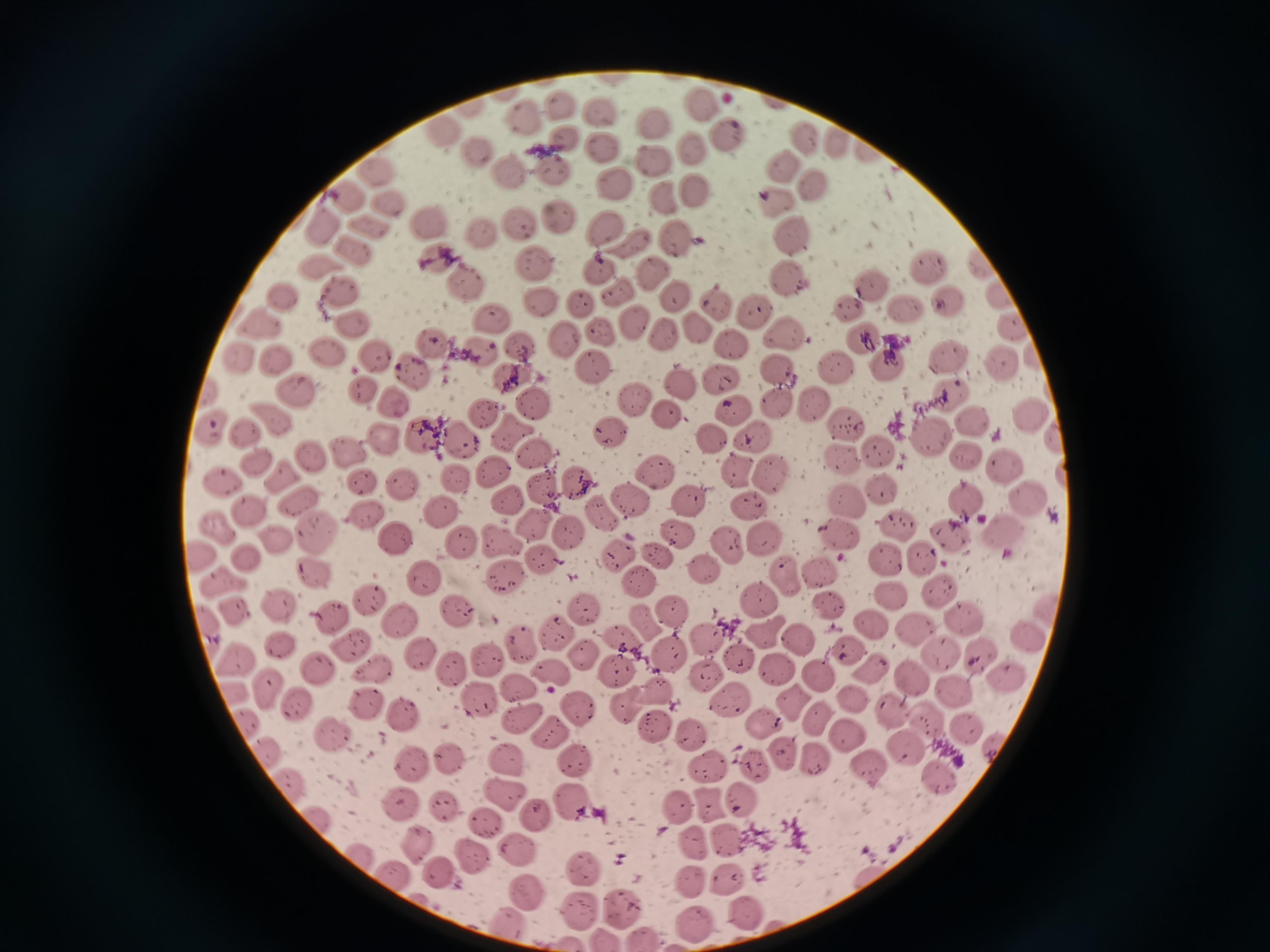 Approximate centers as (x, y) in pixels. Cell locations: (558, 106), (702, 106), (598, 114), (523, 121), (656, 121), (726, 132), (444, 133), (568, 137), (806, 138), (837, 141), (477, 149), (691, 149), (866, 151), (602, 153), (652, 163), (784, 166), (558, 170), (370, 171), (506, 172), (607, 182), (815, 184), (696, 191), (663, 196), (351, 197), (390, 199), (778, 199), (559, 217), (430, 221), (372, 223), (516, 226), (601, 227), (326, 228), (476, 231), (795, 236), (678, 237), (630, 246), (354, 248), (435, 258), (979, 263), (534, 264), (926, 268), (321, 269), (596, 269), (652, 270), (785, 278), (462, 282), (871, 284), (343, 289), (621, 290), (672, 293), (997, 293), (283, 296), (947, 298), (543, 305), (718, 306), (901, 306), (579, 309), (848, 309), (755, 312), (492, 318), (263, 322), (351, 323), (639, 324), (694, 325), (600, 328), (1013, 329), (666, 333), (783, 336), (561, 337), (425, 341), (862, 341), (519, 346), (732, 348), (325, 351), (376, 353), (482, 354), (240, 355), (272, 356), (951, 356), (1035, 356), (1001, 362), (890, 365), (834, 366), (414, 369), (595, 369), (782, 374), (510, 375), (718, 376), (680, 387), (362, 389), (296, 390), (945, 391), (209, 393), (631, 399), (397, 400), (532, 403), (772, 404), (812, 406), (735, 408), (478, 414), (664, 414), (278, 416), (1027, 417), (972, 421), (845, 423), (212, 426), (249, 428), (929, 434), (754, 435), (425, 436), (611, 436), (512, 437), (1052, 438), (712, 439), (382, 443), (460, 446), (342, 450), (882, 450), (540, 454), (307, 456), (962, 457), (837, 458), (256, 460), (1005, 467), (769, 471), (493, 473), (743, 473), (657, 474), (278, 476), (1062, 476), (453, 480), (220, 482), (361, 484), (399, 484), (579, 484), (542, 487), (881, 491), (296, 498), (1029, 498), (964, 499), (692, 500), (508, 503), (629, 503), (751, 504), (845, 505), (249, 506), (438, 513), (364, 515), (603, 515), (898, 521), (534, 526), (676, 526), (218, 527), (1004, 532), (838, 533), (573, 535), (317, 536), (499, 537), (765, 537), (460, 539), (951, 539), (277, 541), (394, 541), (733, 545), (621, 551), (924, 553), (204, 554), (544, 557), (249, 558), (660, 558), (887, 558), (704, 568), (815, 568), (785, 572), (421, 573), (313, 574), (226, 580), (508, 581), (637, 581), (942, 590), (371, 595), (899, 595), (756, 599), (830, 603), (234, 607), (579, 608), (278, 609), (1045, 609), (460, 611), (672, 616), (961, 616), (867, 619), (402, 621), (646, 623), (331, 624), (208, 628), (767, 632), (552, 635), (1025, 636), (706, 637), (801, 638), (622, 639), (276, 643), (849, 645), (354, 646), (520, 648), (979, 651), (421, 652), (582, 654), (942, 654), (236, 657), (672, 657), (494, 660), (742, 660), (777, 664), (372, 666), (316, 670), (550, 670), (452, 671), (868, 671), (621, 672), (815, 673), (909, 675), (1008, 675), (705, 680), (516, 688), (659, 688), (232, 689), (265, 689), (953, 690), (478, 700), (855, 700), (729, 703), (793, 705), (368, 706), (580, 707), (299, 708), (626, 711), (894, 712), (404, 717), (245, 719), (817, 720), (929, 721), (520, 722), (764, 722), (966, 730), (551, 731), (691, 731), (334, 733), (658, 735), (852, 735), (994, 744), (906, 747), (263, 750), (785, 755), (406, 756), (508, 756), (820, 759), (573, 760), (447, 761), (755, 764), (869, 766), (709, 768), (942, 776), (288, 783), (507, 794), (749, 799), (450, 802), (577, 803), (708, 804), (681, 806), (402, 808), (315, 815), (540, 817), (485, 822), (731, 840), (421, 845), (691, 845), (520, 850), (474, 858), (579, 872), (394, 873), (442, 874), (690, 879), (728, 880), (521, 892), (617, 904), (579, 909), (751, 911), (502, 921), (693, 921). Image is 1270×952 pixels. Thin smear of blood. Acquired by smartphone through the microscope eyepiece. Giemsa stain. Single field of view.